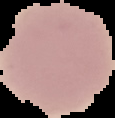
Result: no malaria parasites seen. From a thin blood film. Image is 115×118 pixels. The area outside the segmented cell region is set to black.